Classify this cell by malaria status.
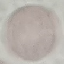
Uninfected.

Acquired by smartphone through the microscope eyepiece. Cell patch, automatically extracted from a larger field of view and resized to 64 × 64 pixels. Giemsa stain. Thin blood film.